Outline each white blood cell.
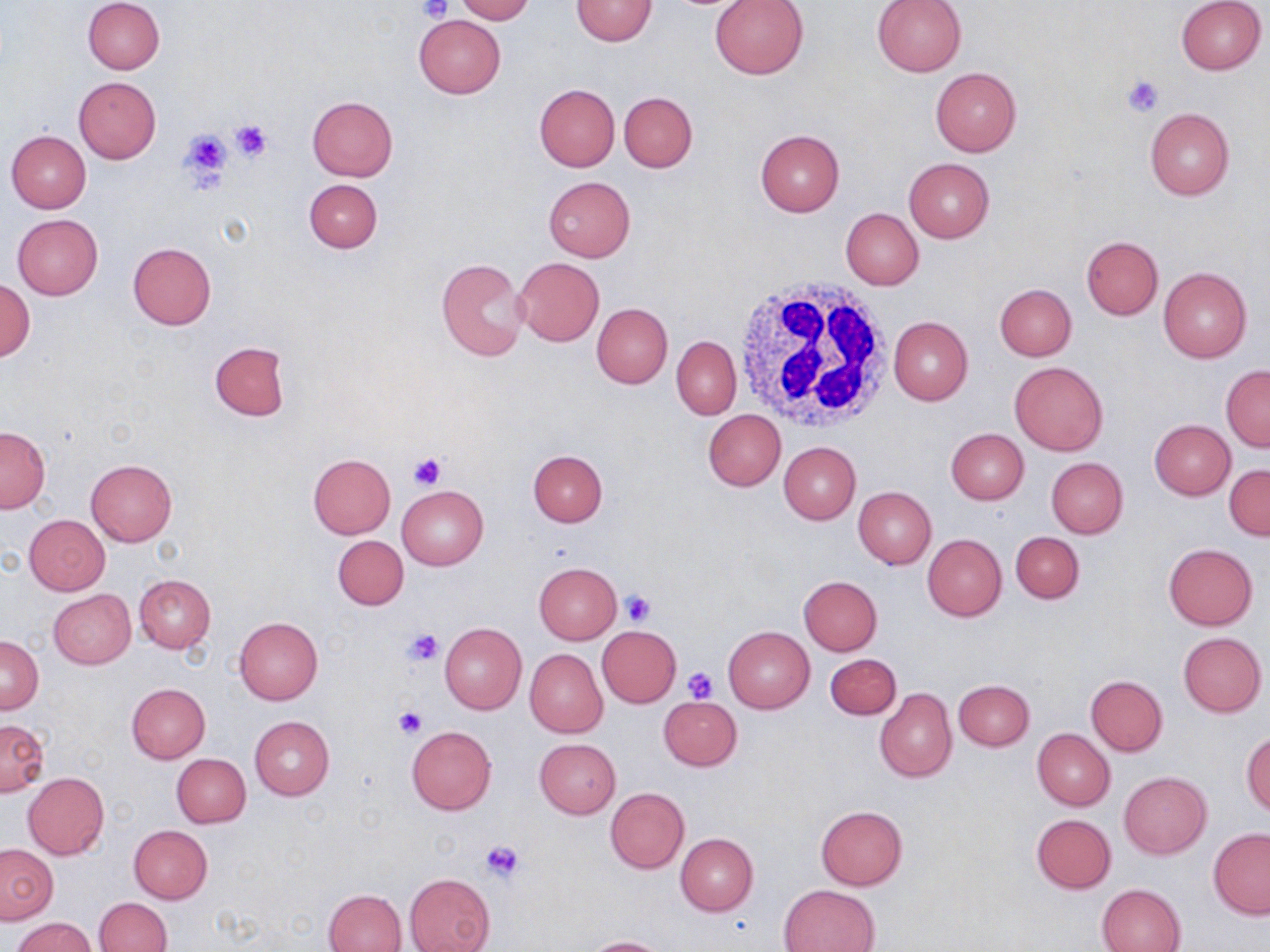

Approximate bounding boxes as (x1,y1)-(x2,y2) corner pairs in pixels.
White blood cells: (729,277)-(896,433).

Uninfected red blood cell locations: (83,0)-(164,75), (455,0)-(535,23), (570,0)-(658,46), (709,0)-(808,80), (872,0)-(966,76), (1175,1)-(1266,75), (413,15)-(506,98), (931,66)-(1022,155), (74,77)-(161,164), (534,83)-(620,171), (619,91)-(697,172), (307,96)-(398,181), (1144,108)-(1234,200), (6,130)-(91,213), (754,130)-(844,217), (904,158)-(994,243), (543,176)-(636,261), (304,179)-(383,252), (840,208)-(924,290), (12,214)-(104,300), (1082,236)-(1163,320), (128,242)-(217,329), (514,257)-(604,346), (437,258)-(532,362), (1158,268)-(1251,362), (1,278)-(35,364), (995,283)-(1077,360), (591,303)-(672,388), (889,316)-(973,405), (671,336)-(742,419), (209,342)-(289,420), (1010,362)-(1107,455), (1221,365)-(1270,451), (703,409)-(785,491), (1150,419)-(1236,500), (0,426)-(50,512), (946,428)-(1029,504), (780,441)-(861,524), (528,449)-(607,527), (308,454)-(395,538), (1046,457)-(1128,538), (86,460)-(177,547), (1225,465)-(1269,541), (396,486)-(488,570), (853,487)-(936,569), (24,515)-(110,595), (1010,532)-(1084,603), (923,534)-(1006,621), (333,535)-(408,609), (1163,543)-(1257,630), (533,562)-(621,645), (134,574)-(216,653), (798,576)-(883,655), (47,589)-(135,670), (234,617)-(323,705), (439,622)-(527,715), (596,625)-(681,706), (723,626)-(814,713), (1178,632)-(1267,716), (0,635)-(43,714), (525,649)-(607,737), (826,653)-(901,719), (1086,675)-(1168,756), (954,679)-(1034,751), (127,684)-(209,763), (875,687)-(956,782), (659,696)-(742,771), (249,715)-(334,800), (2,719)-(48,795), (405,724)-(496,815), (1032,728)-(1115,810), (1241,731)-(1270,815), (535,738)-(621,818), (172,753)-(250,827), (1119,771)-(1211,858), (23,773)-(109,859), (605,787)-(689,873), (815,805)-(908,890), (1031,814)-(1116,893), (129,825)-(212,904), (1208,829)-(1270,919), (676,833)-(758,915), (0,844)-(57,923), (405,873)-(495,952), (1097,883)-(1186,952), (780,884)-(878,952), (324,888)-(407,952), (94,897)-(172,952), (12,917)-(98,952), (582,936)-(672,952). Platelet locations: (418,0)-(451,23), (1120,74)-(1165,115), (231,117)-(273,161), (175,124)-(234,192), (406,451)-(448,490), (620,590)-(654,626), (403,626)-(444,667), (683,667)-(719,704), (392,707)-(428,740), (480,839)-(527,884). Slide-level diagnosis: negative for blood parasites. Image is 1270×952 pixels. Optical microscopy. May-Grünwald-Giemsa stain. Single field of view. Thin blood smear. 1000x magnification.